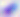

Summary:
  - Modality: micrograph
  - Magnification: 400x
  - Identification: Toxoplasma gondii